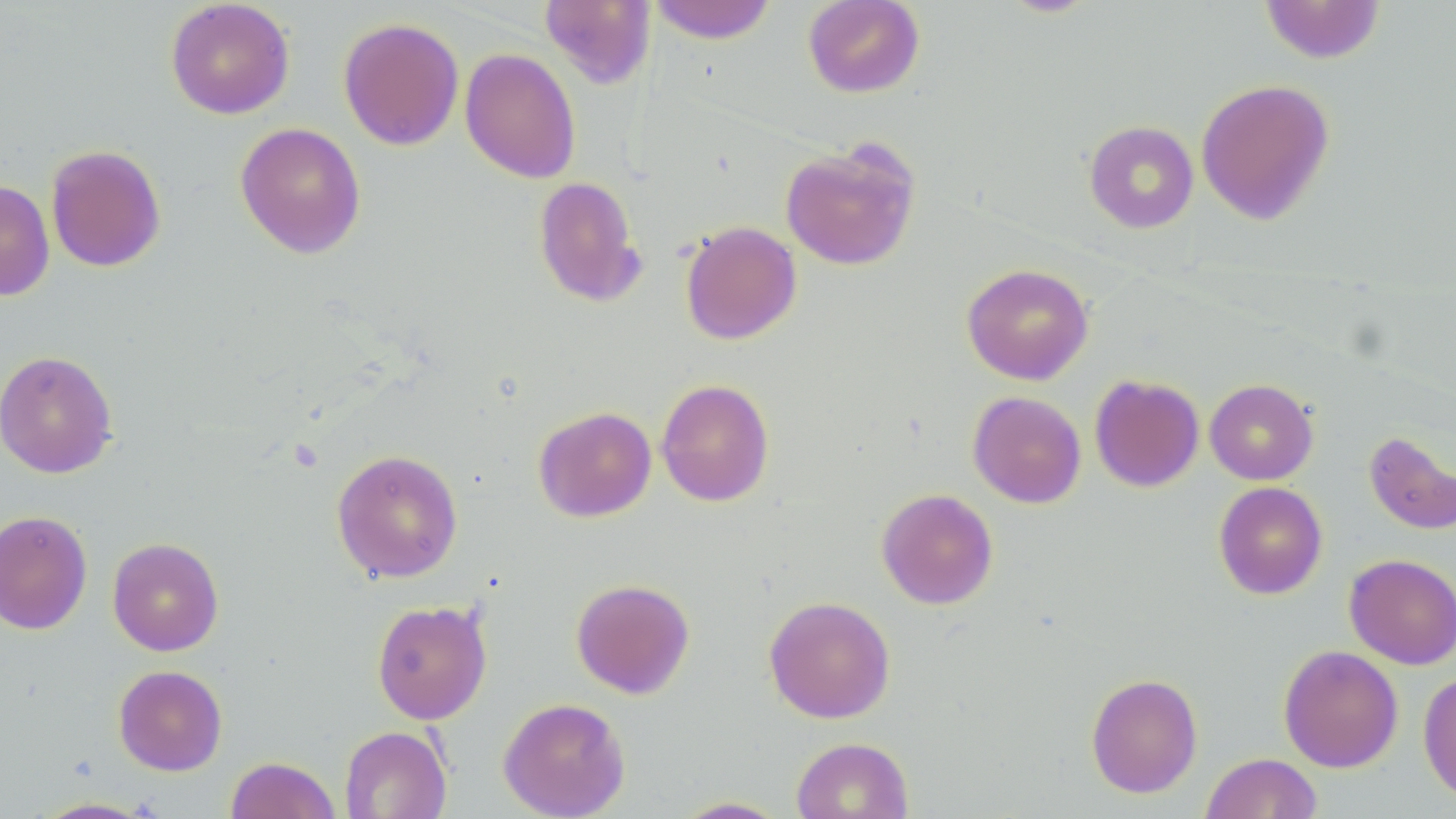

Approximate bounding boxes as named x1/y1/x2/y2 corners in pixels. Uninfected red blood cell locations: (x1=165, y1=0, x2=295, y2=119), (x1=647, y1=0, x2=779, y2=44), (x1=802, y1=0, x2=925, y2=99), (x1=539, y1=1, x2=657, y2=89), (x1=1259, y1=1, x2=1386, y2=63), (x1=338, y1=17, x2=464, y2=151), (x1=460, y1=48, x2=581, y2=183), (x1=1196, y1=78, x2=1335, y2=226), (x1=1083, y1=120, x2=1199, y2=234), (x1=235, y1=122, x2=367, y2=259), (x1=779, y1=138, x2=922, y2=272), (x1=45, y1=144, x2=166, y2=273), (x1=532, y1=175, x2=648, y2=307), (x1=0, y1=179, x2=55, y2=301), (x1=679, y1=220, x2=802, y2=345), (x1=961, y1=263, x2=1094, y2=385), (x1=0, y1=350, x2=118, y2=478), (x1=1089, y1=374, x2=1204, y2=493), (x1=656, y1=378, x2=775, y2=507), (x1=1204, y1=378, x2=1319, y2=485), (x1=968, y1=391, x2=1086, y2=508), (x1=533, y1=406, x2=657, y2=522), (x1=1364, y1=431, x2=1456, y2=536), (x1=331, y1=448, x2=463, y2=583), (x1=1213, y1=481, x2=1327, y2=599), (x1=876, y1=488, x2=998, y2=609), (x1=0, y1=510, x2=93, y2=635), (x1=107, y1=537, x2=224, y2=656), (x1=1344, y1=553, x2=1456, y2=670), (x1=570, y1=578, x2=695, y2=699), (x1=764, y1=595, x2=896, y2=723), (x1=371, y1=599, x2=492, y2=724), (x1=1278, y1=645, x2=1404, y2=772), (x1=113, y1=665, x2=228, y2=775), (x1=1418, y1=670, x2=1456, y2=806), (x1=1085, y1=672, x2=1203, y2=798), (x1=497, y1=697, x2=631, y2=819), (x1=339, y1=725, x2=452, y2=818), (x1=790, y1=736, x2=914, y2=819), (x1=1200, y1=752, x2=1323, y2=818), (x1=225, y1=756, x2=341, y2=819), (x1=671, y1=796, x2=792, y2=818), (x1=30, y1=797, x2=158, y2=818). Slide-level diagnosis: negative for blood parasites. 1000x magnification. Thin blood film. Image is 1456×819 pixels. May-Grünwald-Giemsa stain. Light microscopy. One field of a larger specimen.